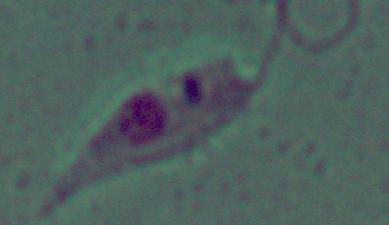

Photomicrograph. 1000x magnification. A Leishmania parasite is shown.